Report the malaria status of this cell.
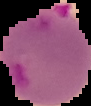
It is parasitized.

Summary:
  - Image type: cell region segmented out of the field of view; surrounding area masked to black
  - Image size: 91×106 pixels
  - Preparation: thin blood smear